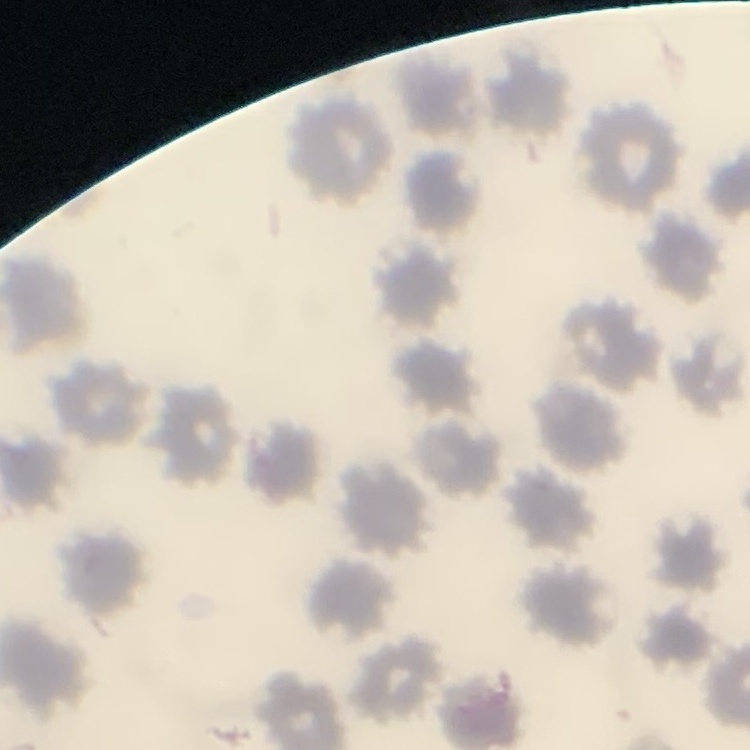

The red blood cells show no rouleaux formation. Field's or Giemsa stain. Square crop of a larger photomicrograph. Thin peripheral smear.